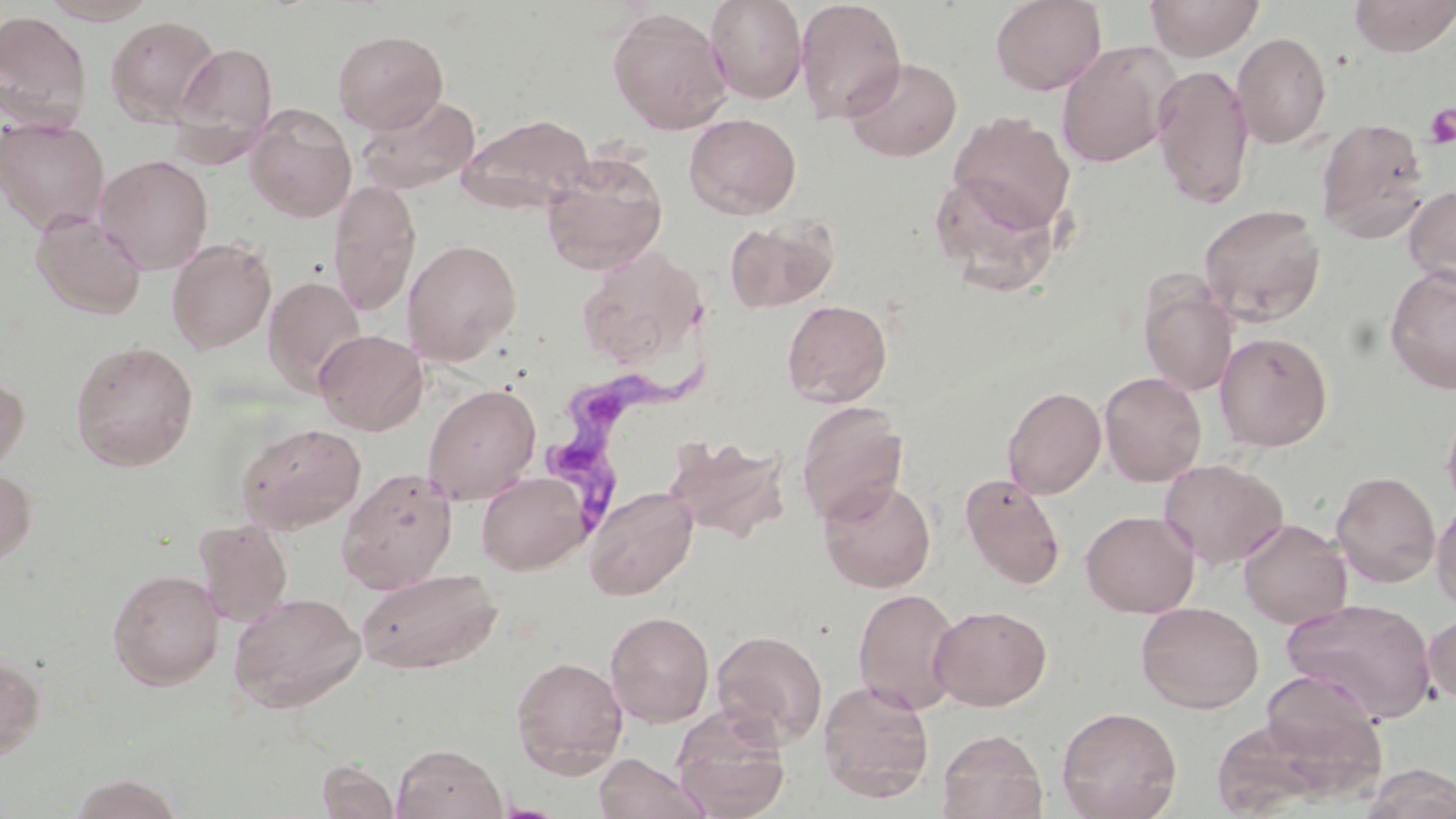
slide-level diagnosis = Trypanosoma brucei
uninfected red blood cell locations = approximate bounding boxes as (x1, y1, x2, y2) in pixels: (40, 0, 158, 25), (705, 0, 808, 104), (795, 0, 907, 124), (990, 0, 1107, 95), (1144, 0, 1265, 60), (1348, 0, 1456, 57), (607, 7, 732, 134), (0, 11, 92, 129), (106, 15, 221, 126), (333, 29, 448, 134), (1232, 31, 1331, 148), (172, 41, 278, 156), (1057, 43, 1176, 169), (843, 56, 963, 162), (1151, 64, 1256, 210), (357, 93, 480, 195), (245, 106, 356, 222), (946, 112, 1077, 235), (457, 113, 595, 213), (684, 113, 802, 219), (0, 116, 110, 234), (1315, 116, 1430, 242), (96, 154, 214, 274), (541, 155, 668, 275), (928, 168, 1065, 295), (328, 178, 421, 318), (1404, 184, 1456, 288), (1198, 203, 1327, 326), (30, 211, 147, 320), (724, 218, 838, 313), (167, 238, 277, 354), (403, 239, 522, 364), (578, 242, 705, 365), (1384, 265, 1456, 395), (263, 275, 367, 396), (1139, 280, 1239, 397), (782, 299, 893, 407), (314, 329, 427, 435), (1214, 331, 1333, 452), (70, 340, 198, 472), (0, 369, 30, 473), (1098, 371, 1207, 486), (423, 383, 542, 505), (1002, 385, 1107, 499), (1441, 398, 1456, 515), (795, 400, 909, 525), (237, 422, 366, 533), (665, 435, 792, 541), (1158, 457, 1289, 570), (0, 467, 37, 566), (336, 467, 457, 593), (476, 470, 591, 575), (1331, 471, 1441, 588), (960, 473, 1066, 590), (818, 478, 936, 592), (583, 484, 699, 600), (1431, 495, 1456, 614), (1081, 510, 1199, 618), (194, 518, 293, 626), (1238, 518, 1352, 629), (356, 568, 502, 675), (108, 569, 225, 689), (852, 587, 963, 714), (227, 590, 366, 713), (1282, 597, 1438, 722), (1136, 601, 1264, 713), (930, 605, 1052, 710), (605, 610, 715, 726), (1422, 611, 1456, 705), (711, 629, 828, 747), (0, 651, 45, 761), (511, 655, 628, 777), (1255, 669, 1389, 779), (818, 678, 935, 802), (1056, 705, 1183, 819), (671, 708, 792, 819), (937, 729, 1049, 819), (392, 743, 507, 819), (593, 753, 709, 819), (317, 759, 399, 819), (1358, 763, 1456, 819), (67, 773, 185, 819)
preparation = thin blood film
stain = May-Grünwald-Giemsa
modality = optical microscopy
platelet locations = approximate bounding boxes as (x1, y1, x2, y2) in pixels: (1424, 103, 1456, 149)
Trypanosoma brucei locations = approximate bounding boxes as (x1, y1, x2, y2) in pixels: (543, 356, 709, 553)
magnification = 1000x
field of view = one of a larger specimen
image size = 1456×819 pixels